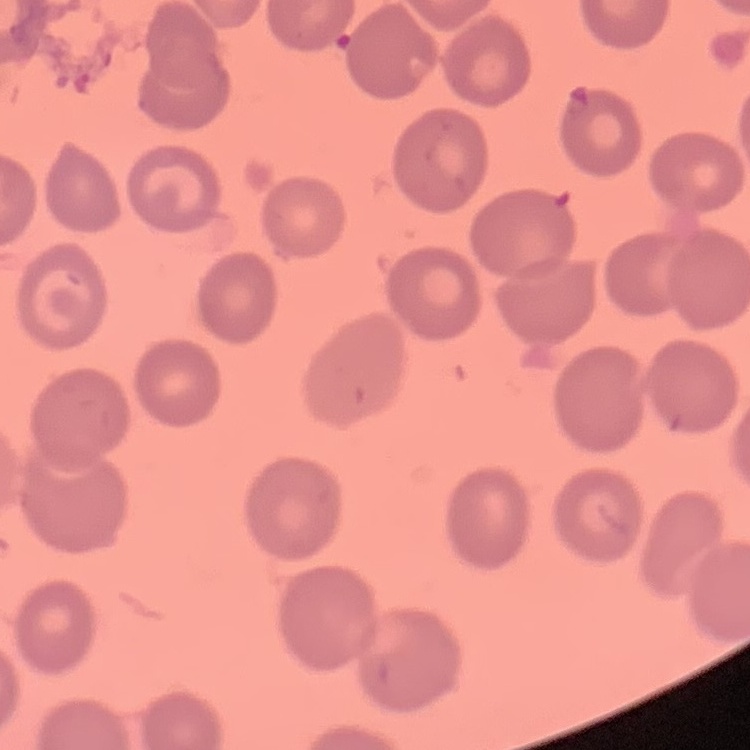

red blood cell morphology = no rouleaux formation
image type = square crop of a larger photomicrograph
preparation = thin peripheral smear
stain = Field's or Giemsa